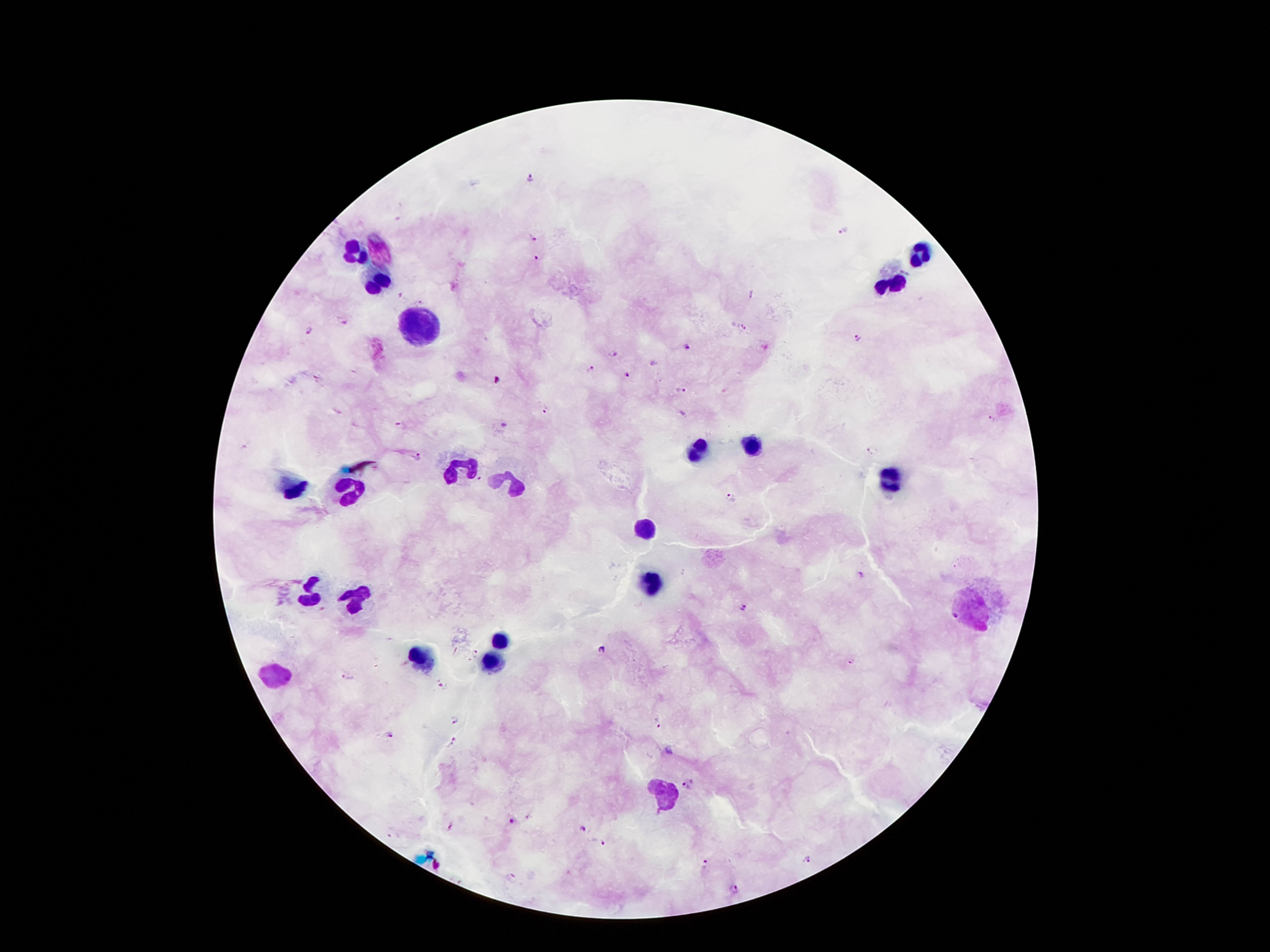 Approximate centers as (x, y) in pixels. Malaria parasite locations: (530, 178), (843, 230), (531, 237), (539, 258), (752, 294), (344, 320), (742, 328), (307, 330), (858, 338), (688, 348), (614, 355), (654, 363), (591, 368), (626, 375), (498, 381), (678, 391), (545, 410), (502, 425), (417, 457), (730, 495), (859, 574), (744, 607), (600, 651), (475, 655), (852, 661), (347, 677), (443, 683), (454, 719), (656, 721), (391, 734), (452, 743), (687, 784), (511, 820), (583, 828), (601, 842), (808, 859), (705, 862), (509, 877), (734, 888). Leukocyte locations: (356, 251), (379, 252), (917, 256), (376, 281), (893, 284), (414, 330), (750, 447), (700, 449), (463, 467), (890, 482), (513, 485), (297, 492), (351, 492), (647, 534), (651, 583), (311, 593), (357, 597), (961, 610), (498, 643), (424, 659), (494, 661), (278, 675), (665, 793). Image is 1270×952 pixels. Giemsa-stained preparation. Thick blood smear. Smartphone photograph taken through the microscope eyepiece. Patient malaria status: positive for Plasmodium falciparum. 100x magnification. One field from this slide.